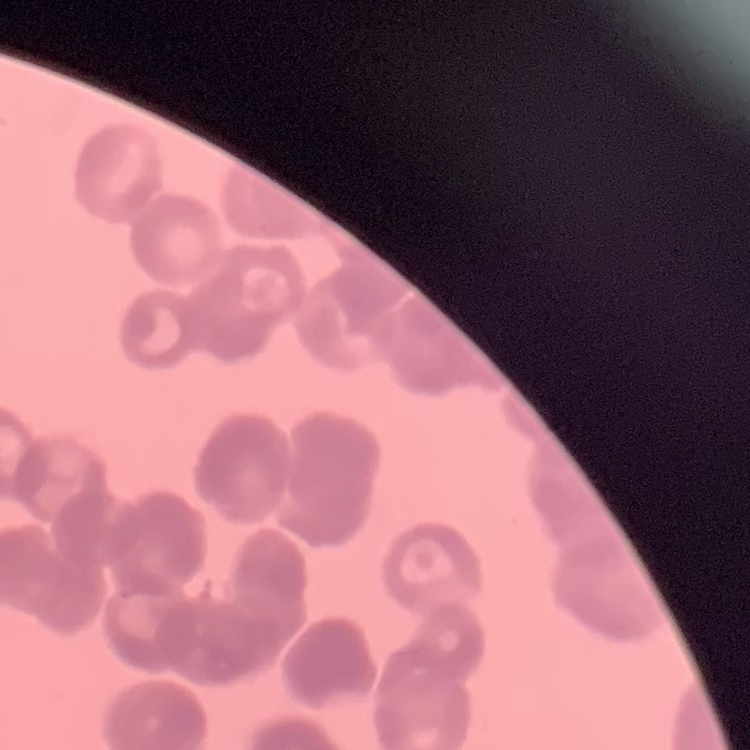

erythrocyte morphology = rouleaux formation
image type = one tile cut from a larger photomicrograph
stain = Field's or Giemsa
preparation = thin peripheral smear